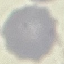

Summary:
  - Malaria status: uninfected
  - Image type: automatically extracted cell patch, resized to 64 × 64 pixels
  - Stain: Giemsa
  - Capture: smartphone camera at the microscope eyepiece
  - Preparation: thin blood film